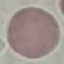
Result: negative for malaria parasites. Thin blood smear. Cell patch, automatically extracted from a larger field of view and resized to 64 × 64 pixels. Photographed with a smartphone camera at the microscope eyepiece. Giemsa-stained preparation.